Locate every Plasmodium parasite.
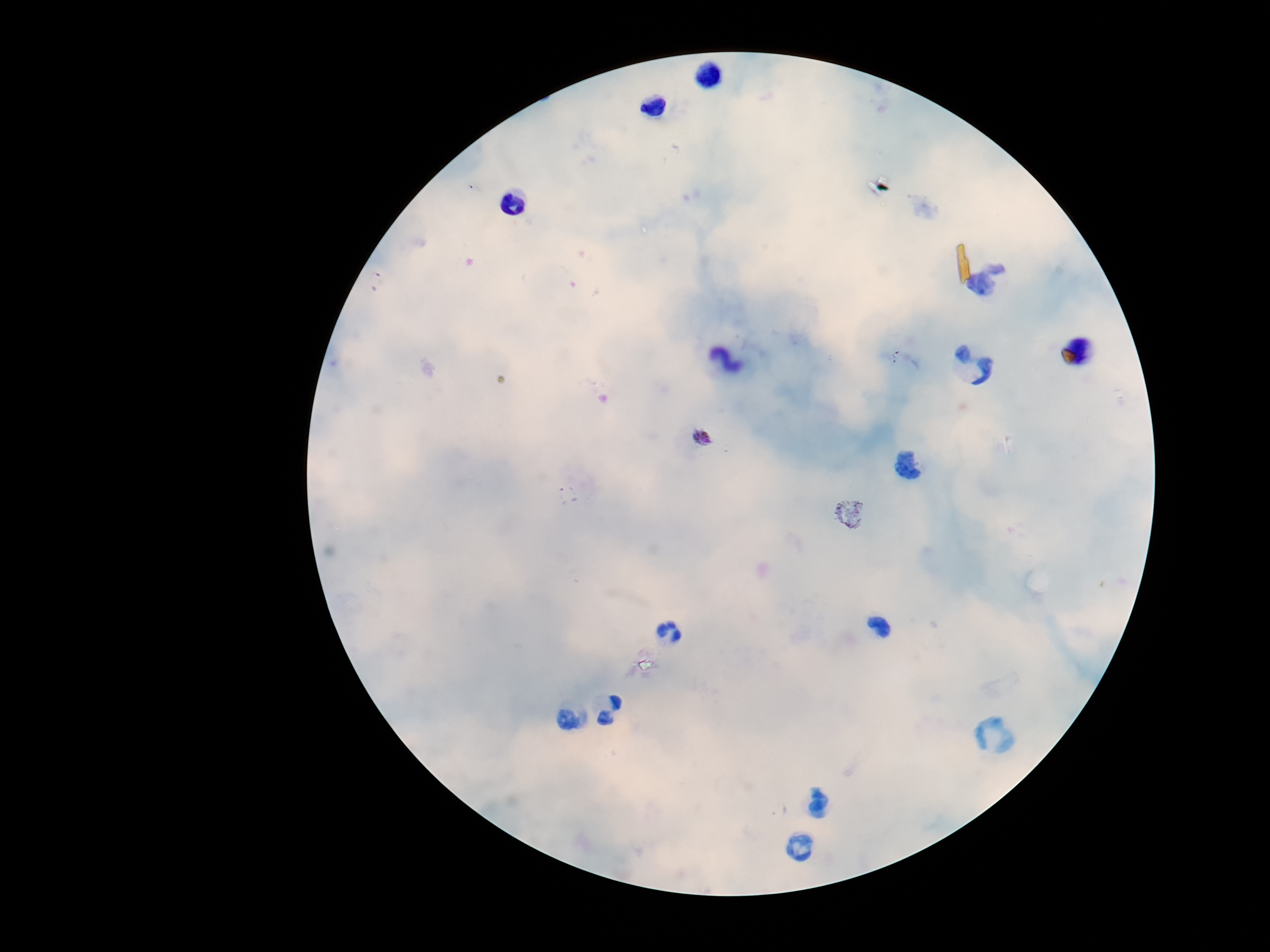
Approximate object centers, in pixels from the top-left corner.
Plasmodium parasites: (x=701, y=436), (x=906, y=467), (x=567, y=494), (x=848, y=510).

Image is 1270×952 pixels. Thick blood film. Giemsa stain. Patient malaria status: positive. Photographed through the microscope eyepiece with a smartphone camera. Single field of view. 100x magnification.